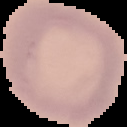

Summary:
  - Image type: segmented cell region with the area outside set to black
  - Malaria status: uninfected
  - Preparation: thin blood smear
  - Image size: 127×127 pixels